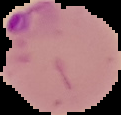

Segmented cell region on a black background. From a thin blood film. Malaria status: parasitized. Image is 121×115 pixels.